Locate every blood parasite and identify its species.
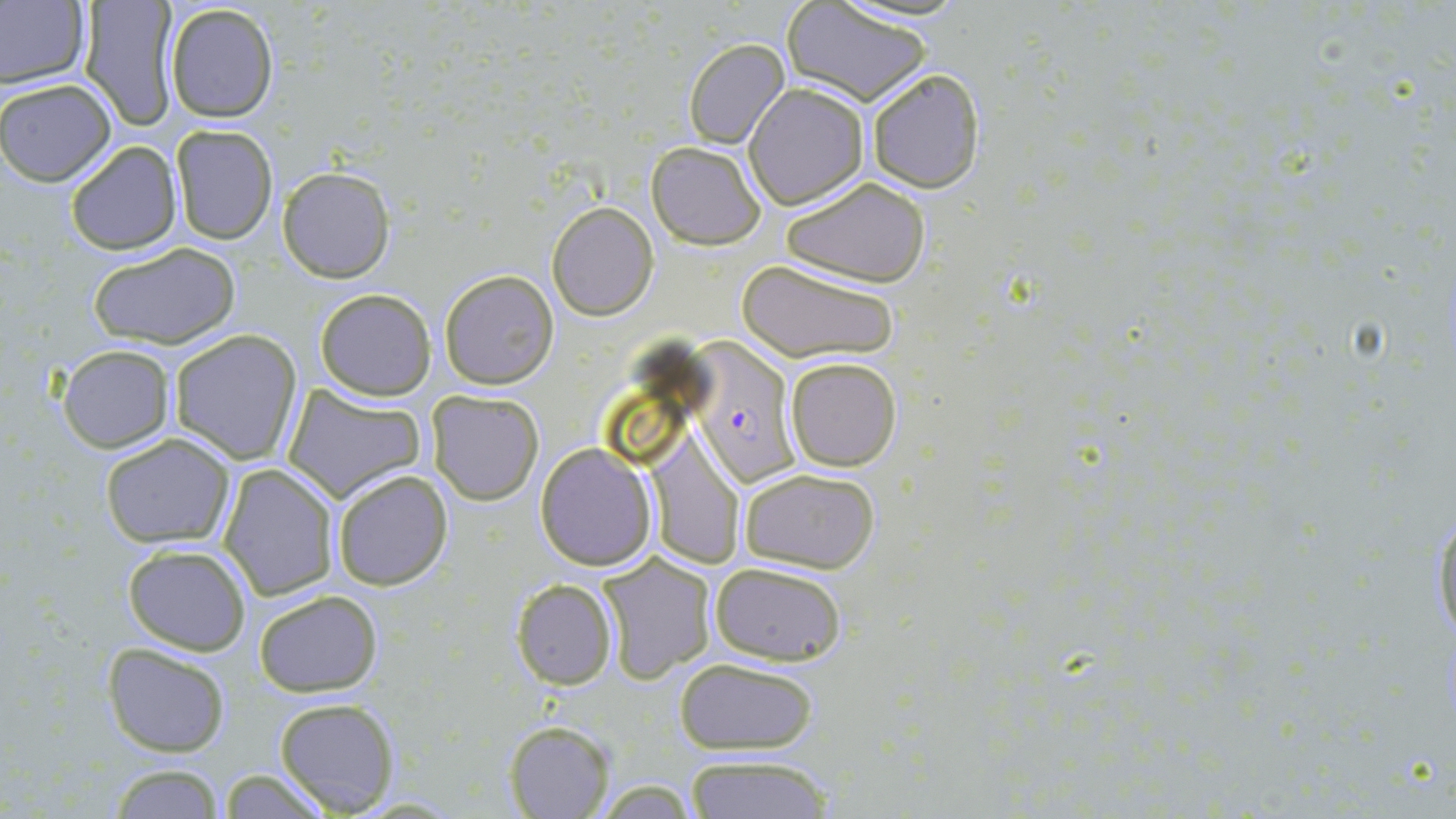

Approximate bounding boxes as (x1,y1)-(x2,y2) corner pairs in pixels.
Plasmodium falciparum-infected red blood cells: (693,344)-(793,488).
No Plasmodium ovale, Plasmodium malariae, Plasmodium vivax, Babesia divergens, or Trypanosoma brucei observed.

Uninfected red blood cell locations: (0,0)-(89,92), (77,0)-(179,131), (163,2)-(279,124), (783,3)-(933,107), (683,37)-(789,149), (866,65)-(985,193), (0,77)-(117,185), (744,82)-(869,209), (170,125)-(278,244), (64,139)-(183,256), (647,141)-(765,248), (278,166)-(394,282), (781,176)-(932,288), (547,202)-(659,321), (87,243)-(242,349), (738,257)-(900,364), (438,270)-(558,389), (313,287)-(437,401), (170,330)-(302,464), (56,344)-(175,454), (785,356)-(902,471), (283,383)-(426,504), (426,389)-(544,504), (98,432)-(236,548), (534,443)-(657,570), (649,444)-(747,569), (219,463)-(339,601), (737,466)-(881,574), (331,469)-(453,591), (1429,492)-(1456,658), (121,543)-(253,656), (596,553)-(716,683), (711,563)-(847,665), (511,578)-(617,689), (254,589)-(382,696), (101,643)-(231,756), (674,659)-(820,754), (273,696)-(400,815), (504,720)-(613,817), (683,756)-(835,818), (104,764)-(226,818), (214,767)-(334,819). Slide-level diagnosis: Plasmodium falciparum. Captured at 1000x magnification. One field of a larger specimen. Image is 1456×819 pixels. May-Grünwald-Giemsa stain. Thin blood smear. Light microscopy.